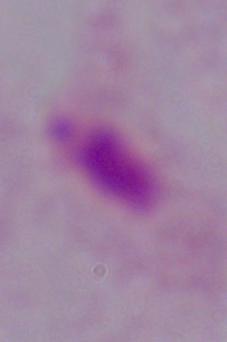

magnification = 1000x
modality = micrograph
identification = trichomonad